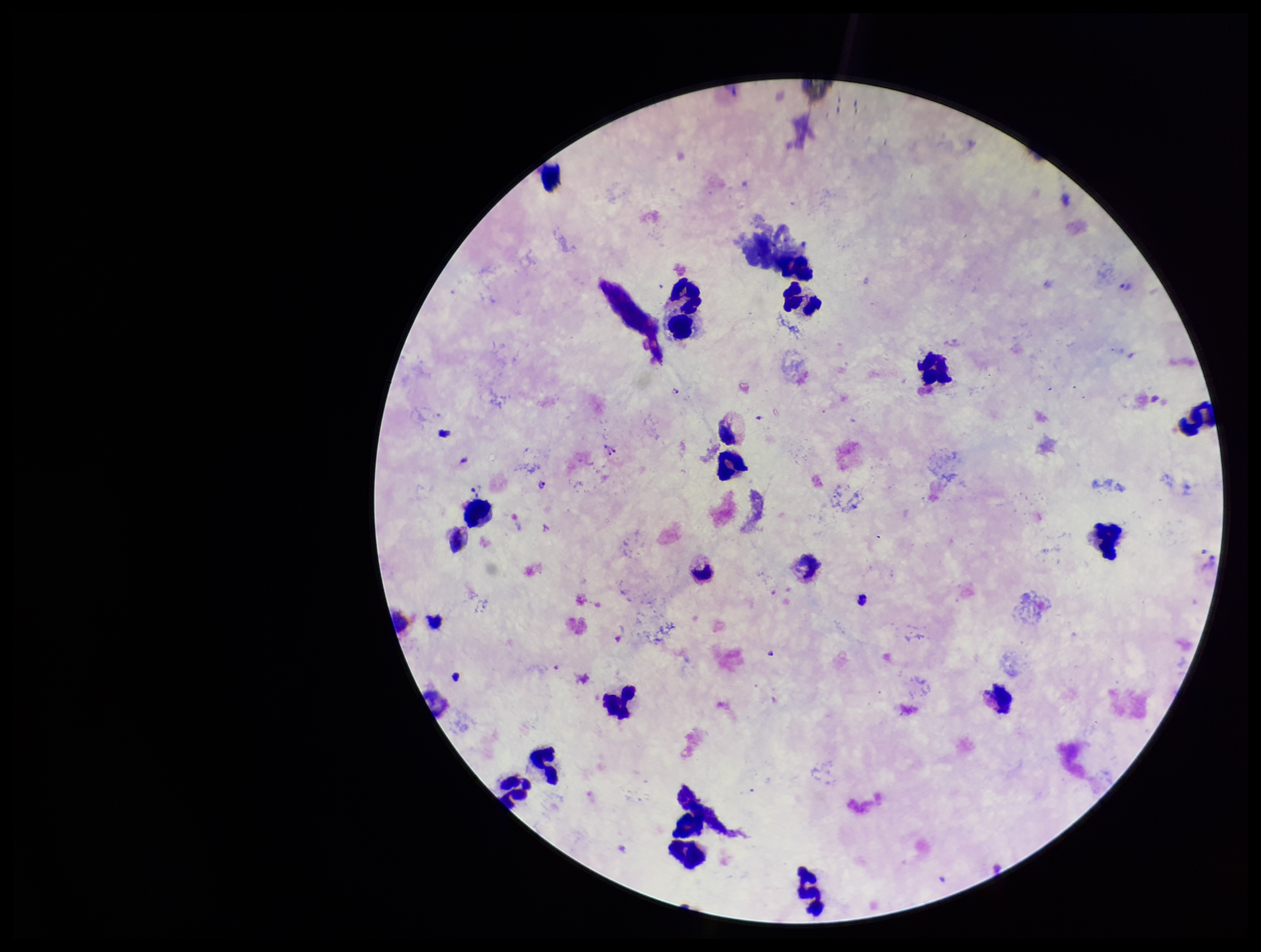

Summary:
  - Stain: Giemsa
  - Patient malaria status: positive
  - Plasmodium parasites: seen
  - Field of view: one from this slide
  - Preparation: thick
  - Parasite count: 5
  - Capture: smartphone photograph through the microscope eyepiece
  - Species reported for this patient: Plasmodium vivax
  - Leukocyte count: 19
  - Image size: 1261×952 pixels